Locate every Plasmodium parasite.
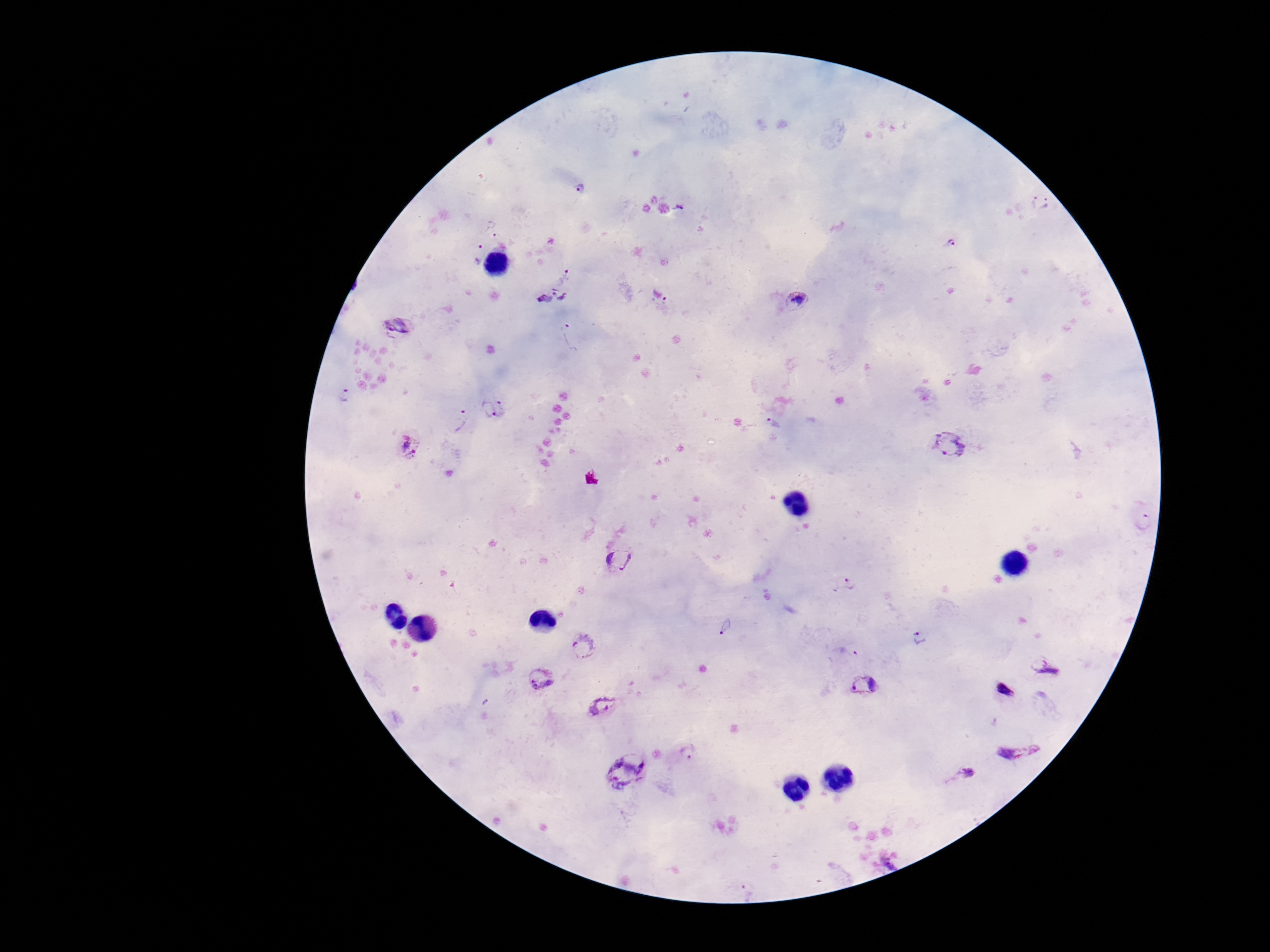
Approximate object centers, in pixels from the top-left corner.
Plasmodium parasites: (x=579, y=188), (x=1040, y=205), (x=680, y=206), (x=492, y=225), (x=949, y=242), (x=474, y=251), (x=567, y=271), (x=551, y=294), (x=795, y=300), (x=661, y=309), (x=396, y=326), (x=344, y=396), (x=492, y=407), (x=457, y=420), (x=772, y=425), (x=407, y=446), (x=950, y=446), (x=1145, y=524), (x=622, y=560), (x=844, y=583), (x=726, y=628), (x=918, y=638), (x=582, y=644), (x=848, y=651), (x=1048, y=668), (x=544, y=680), (x=864, y=689), (x=1004, y=690), (x=604, y=705), (x=1018, y=749), (x=688, y=750), (x=628, y=771), (x=965, y=772), (x=888, y=864).

{
  "capture": "smartphone camera through the microscope eyepiece",
  "patient_malaria_status": "positive",
  "magnification": "100x",
  "stain": "Giemsa",
  "preparation": "thick blood smear",
  "image_size": "1270×952 pixels",
  "field_of_view": "one from this slide"
}